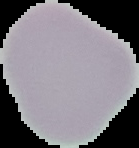
{
  "preparation": "thin blood film",
  "image_size": "139×148 pixels",
  "image_type": "cell region segmented out of the field of view; surrounding area masked to black",
  "malaria_status": "uninfected"
}